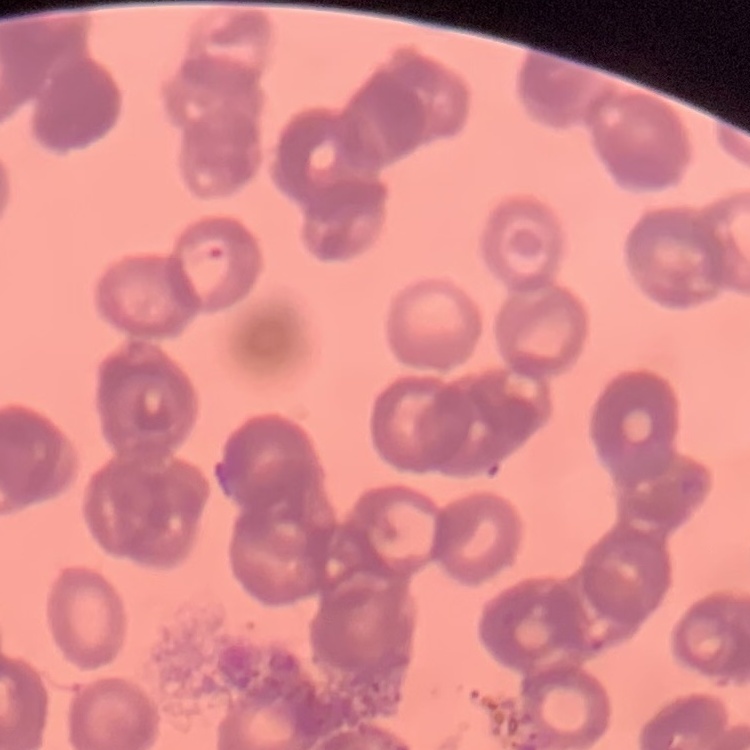
Summary:
  - Erythrocyte morphology: rouleaux formation
  - Stain: Field's or Giemsa
  - Preparation: thin blood film
  - Image type: one tile cut from a larger photomicrograph